Give the position of every malaria parasite.
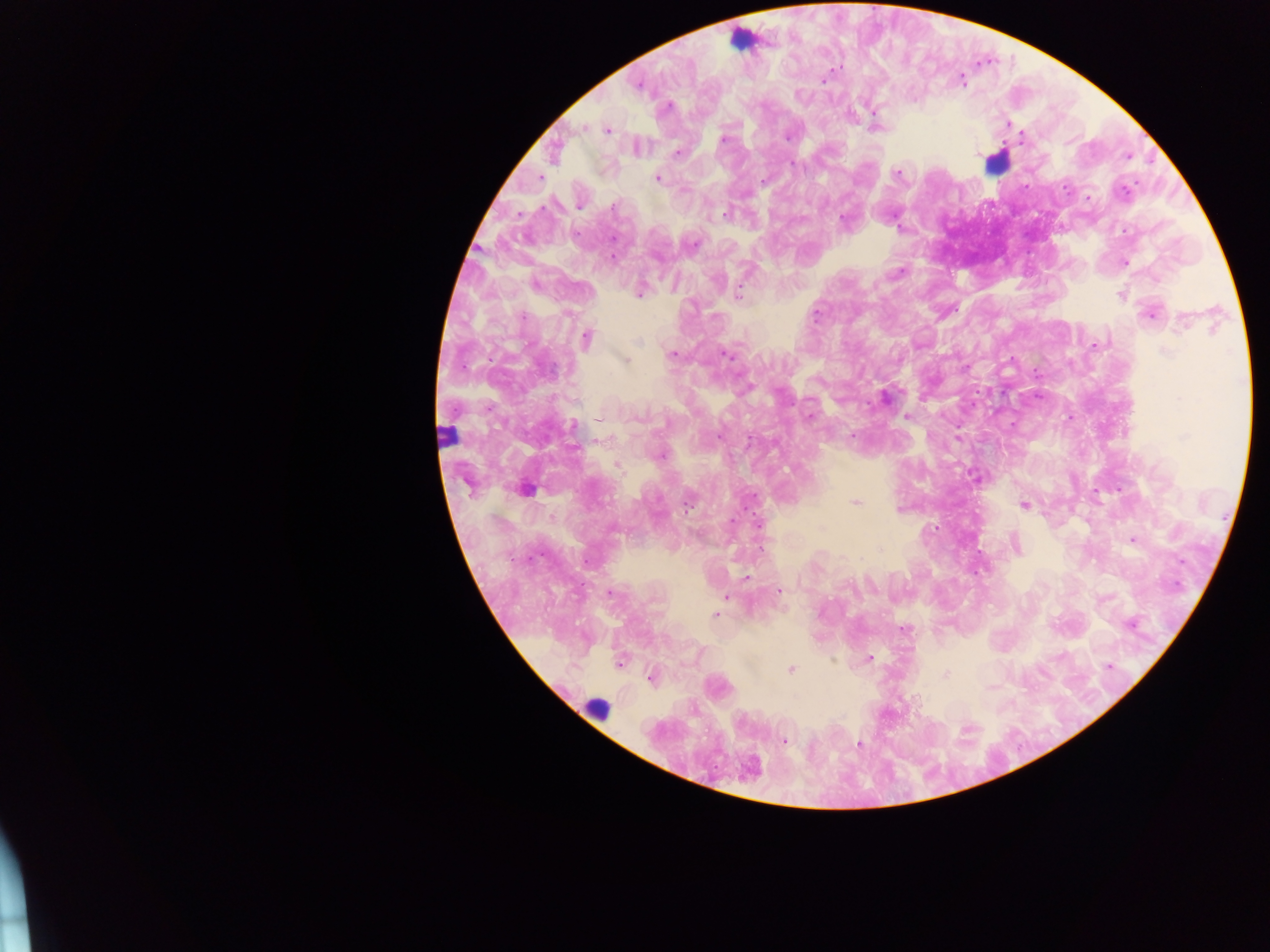
Approximate centers as x y in pixels.
Malaria parasites: 960 79; 822 80; 637 85; 668 107; 582 127; 874 128; 607 130; 788 135; 1021 138; 723 140; 636 147; 555 150; 977 151; 676 153; 1128 156; 896 172; 538 178; 657 178; 1086 197; 579 205; 728 213; 844 220; 613 257; 1124 263; 535 283; 640 291; 1122 295; 738 296; 1150 312; 587 338; 672 354; 727 354; 625 360; 884 398; 809 417; 906 417; 1012 424; 573 426; 957 438; 660 454; 617 464; 975 476; 1119 489; 855 503; 1024 505; 1132 540; 1016 545; 746 577; 778 590; 609 592; 726 597; 716 614; 1130 623; 904 628; 868 658; 619 664; 1108 666; 790 669; 945 674; 651 677; 782 740; 859 744; 748 768.

leukocyte locations = approximate centers as x y in pixels: 743 40; 995 163; 447 436; 524 489; 597 708
capture = mobile-phone photograph through a microscope
country = Ghana
field of view = single
image size = 1270×952 pixels
preparation = thick blood smear